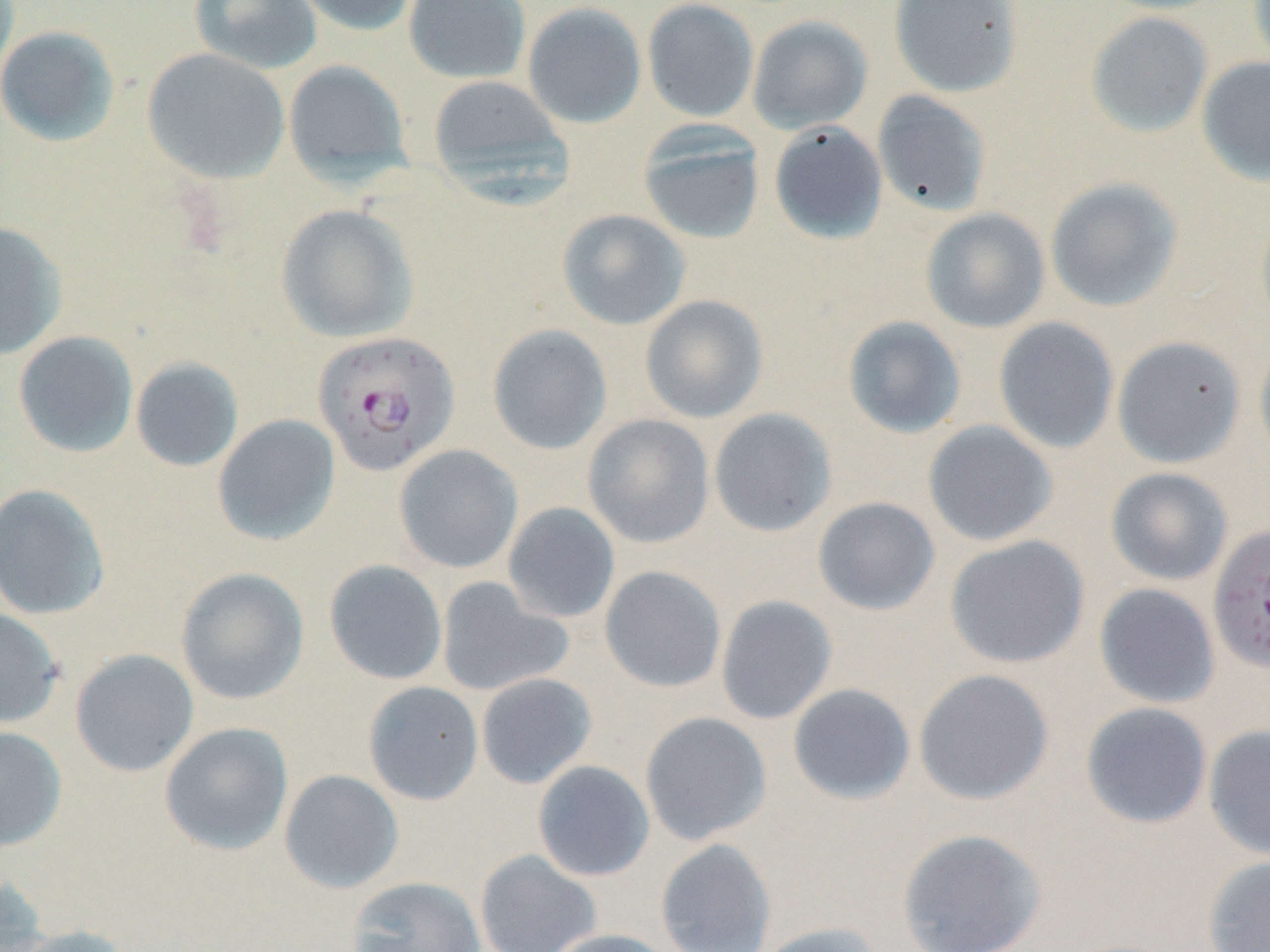

Summary:
  - Coordinate format: approximate bounding boxes as (x1,y1)-(x2,y2) corner pairs in pixels
  - Plasmodium falciparum-infected red blood cell locations: (313,330)-(460,477), (1207,524)-(1270,673)
  - Uninfected red blood cell locations: (189,0)-(324,75), (287,0)-(419,36), (403,0)-(531,84), (642,0)-(759,122), (889,0)-(1026,98), (1097,0)-(1229,14), (1248,0)-(1270,73), (521,1)-(647,129), (1086,12)-(1214,138), (747,15)-(873,134), (0,25)-(121,146), (142,48)-(290,184), (1196,56)-(1270,186), (283,60)-(412,187), (427,74)-(571,191), (872,90)-(991,216), (769,122)-(888,244), (638,123)-(766,245), (1044,177)-(1184,312), (275,204)-(419,343), (557,208)-(691,330), (920,208)-(1051,333), (0,220)-(68,360), (639,295)-(769,424), (842,315)-(967,438), (993,317)-(1119,454), (487,324)-(613,455), (13,331)-(139,458), (1112,336)-(1247,469), (1254,338)-(1270,471), (130,357)-(244,472), (708,407)-(838,537), (212,414)-(341,546), (582,414)-(715,549), (921,420)-(1059,547), (394,444)-(523,574), (1105,466)-(1234,586), (0,483)-(111,620), (812,496)-(941,616), (502,502)-(620,624), (944,535)-(1090,669), (323,559)-(448,685), (599,566)-(727,693), (175,567)-(310,705), (436,576)-(574,697), (1094,583)-(1221,709), (715,595)-(838,725), (0,607)-(65,729), (69,648)-(200,778), (914,668)-(1054,805), (475,673)-(597,789), (363,681)-(484,806), (787,683)-(916,806), (1080,702)-(1213,830), (639,711)-(773,845), (159,722)-(294,855), (1203,724)-(1270,862), (0,725)-(67,850), (532,760)-(655,882), (279,769)-(404,894), (896,827)-(1048,952), (655,838)-(777,952), (475,849)-(602,952), (1202,856)-(1270,952), (0,872)-(53,951), (347,876)-(486,952), (753,921)-(888,952), (7,924)-(136,952), (542,928)-(679,952)
  - Slide-level diagnosis: Plasmodium falciparum
  - Field of view: single
  - Image size: 1270×952 pixels
  - Magnification: 1000x
  - Preparation: thin blood film
  - Modality: optical microscopy
  - Stain: May-Grünwald-Giemsa